Which red blood cells are P. falciparum-infected, and which are of indeterminate infection status?
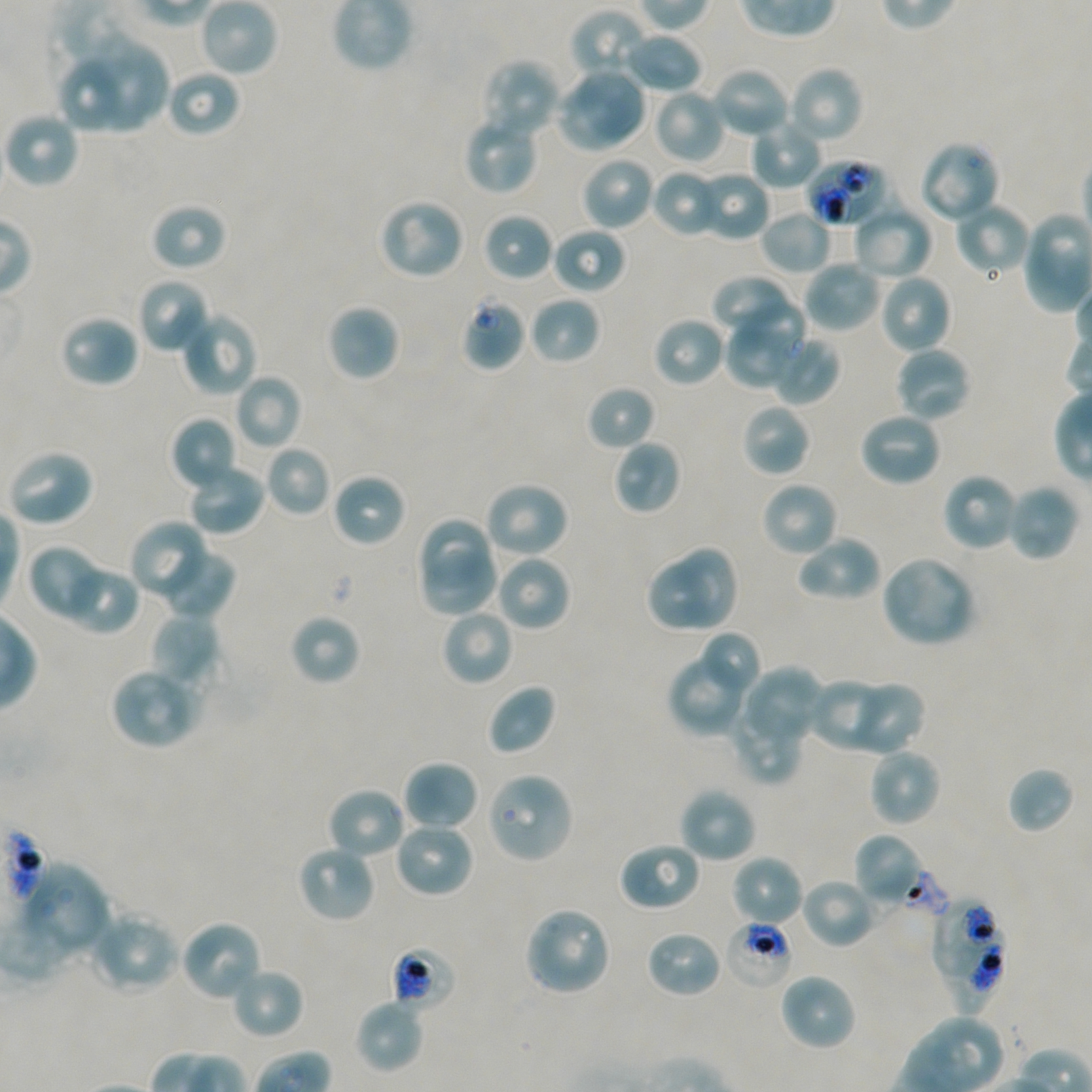
Approximate bounding boxes as (x1, y1, x2, y2) in pixels. Not every red blood cell is marked. A life-cycle stage — or a range of stages, where the recorded stages span more than one — follows each staged infected red blood cell.
Infected red blood cells: (932, 895, 996, 979) trophozoite.
Red blood cells of indeterminate infection status: (805, 158, 892, 228), (460, 294, 527, 371), (887, 867, 948, 916), (724, 917, 795, 990), (942, 927, 1006, 1017), (390, 944, 458, 1012).

Summary:
  - Locations of uninfected red blood cells: (200, 0, 278, 77), (570, 9, 651, 83), (623, 31, 703, 94), (77, 35, 168, 131), (481, 58, 562, 140), (57, 62, 121, 133), (711, 65, 792, 139), (786, 65, 864, 145), (166, 68, 242, 138), (577, 68, 647, 143), (554, 83, 634, 150), (654, 88, 727, 164), (3, 111, 80, 189), (462, 113, 539, 195), (749, 117, 822, 189), (917, 141, 1001, 224), (580, 156, 655, 231), (651, 168, 724, 238), (694, 170, 772, 242), (378, 197, 466, 280), (953, 201, 1032, 277), (150, 202, 228, 271), (852, 202, 934, 281), (760, 208, 832, 275), (481, 212, 554, 283), (551, 227, 627, 294), (802, 258, 883, 333), (710, 273, 789, 334), (878, 273, 953, 354), (136, 277, 212, 355), (528, 295, 601, 366), (734, 299, 809, 365), (327, 303, 400, 382), (180, 310, 258, 397), (58, 314, 140, 388), (653, 316, 727, 388), (723, 327, 795, 389), (771, 335, 840, 405), (894, 346, 972, 422), (234, 372, 304, 450), (586, 384, 656, 452), (741, 403, 812, 477), (858, 410, 943, 487), (170, 416, 238, 492), (612, 439, 682, 515), (264, 444, 331, 517), (5, 448, 94, 528), (187, 463, 267, 537), (941, 472, 1020, 552), (331, 473, 406, 548), (760, 480, 839, 559), (483, 481, 570, 560), (1004, 484, 1080, 563), (416, 516, 495, 590), (130, 520, 211, 601), (795, 534, 882, 603), (674, 543, 742, 632), (26, 545, 107, 622), (157, 547, 236, 620), (416, 550, 502, 617), (495, 553, 572, 632), (879, 555, 976, 647), (644, 561, 716, 634), (58, 563, 139, 635), (440, 608, 514, 687), (289, 613, 361, 686), (151, 614, 221, 688), (698, 630, 763, 697), (668, 650, 752, 735), (742, 666, 825, 746), (110, 667, 200, 750), (809, 677, 888, 752), (845, 681, 926, 755), (486, 684, 557, 756), (727, 695, 805, 785), (868, 748, 943, 827), (403, 759, 479, 832), (1006, 765, 1076, 835), (485, 771, 574, 864), (326, 786, 407, 861), (678, 786, 758, 864), (393, 820, 475, 899), (853, 833, 930, 910), (618, 840, 702, 912), (296, 844, 376, 924), (729, 853, 805, 928), (20, 862, 111, 960), (801, 877, 879, 949), (524, 906, 613, 996), (89, 912, 179, 994), (179, 919, 263, 1003), (644, 928, 723, 998), (230, 964, 304, 1040), (778, 971, 858, 1052), (354, 999, 425, 1074)
  - Objective: 100x, oil immersion, numerical aperture 1.45
  - Preparation: thin blood film
  - Image size: 1092×1092 pixels
  - Donor blood group: A+/O+
  - Stain: Giemsa
  - Culture: in-vitro P. falciparum strain NF54, static
  - Field of view: one from this slide